Give the extent of all Plasmodium falciparum-infected red blood cells.
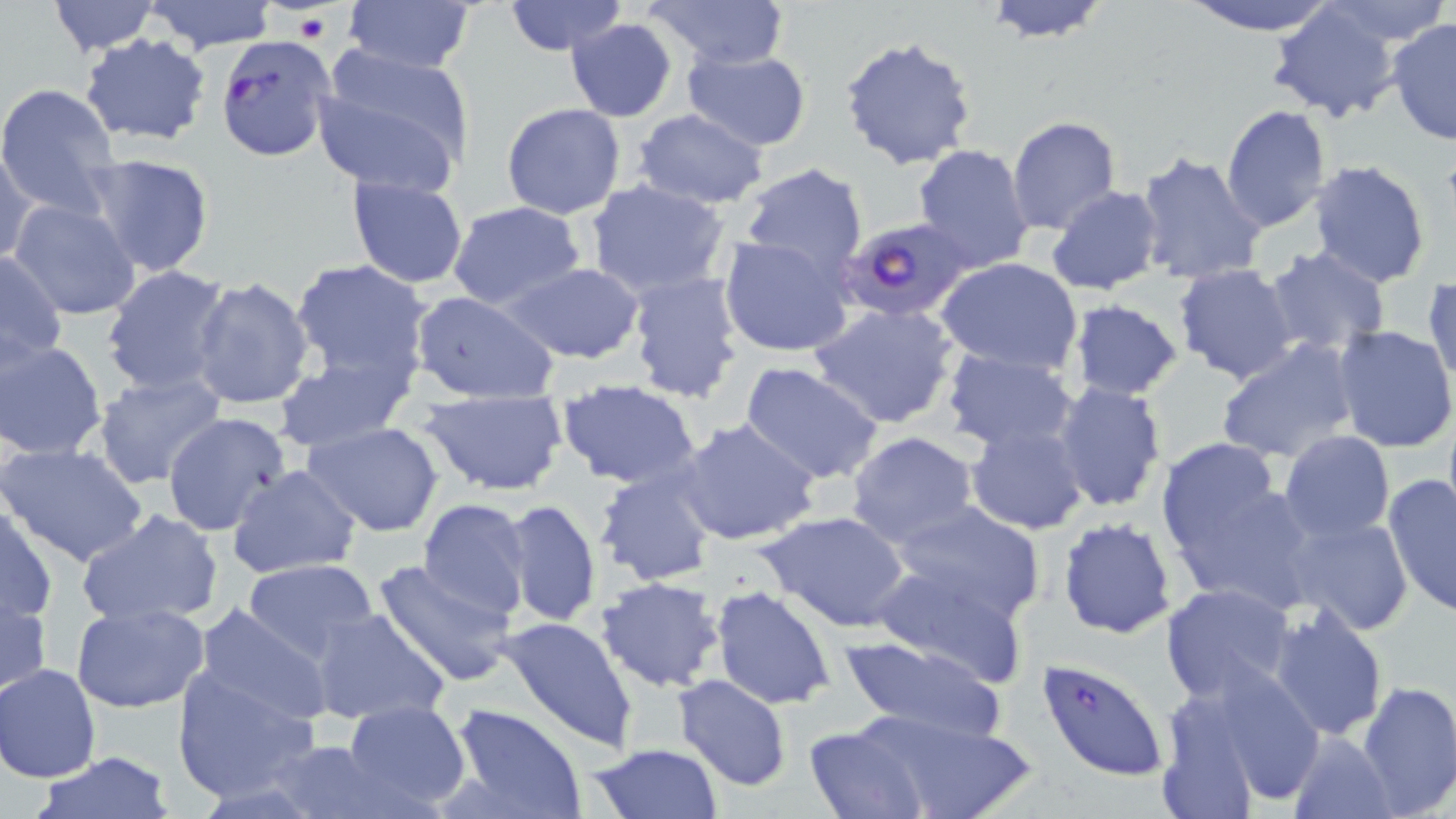
Approximate bounding boxes as (x1,y1)-(x2,y2) corner pairs in pixels.
Plasmodium falciparum-infected red blood cells: (216,35)-(334,161), (838,216)-(974,322), (1037,657)-(1170,782).

slide-level diagnosis = Plasmodium falciparum
uninfected red blood cell locations = approximate bounding boxes as (x1,y1)-(x2,y2) corner pairs in pixels: (47,0)-(162,56), (138,0)-(281,53), (502,0)-(628,55), (644,0)-(789,70), (979,0)-(1115,42), (1179,0)-(1341,36), (342,1)-(477,76), (1319,1)-(1453,48), (1266,4)-(1402,125), (565,16)-(678,121), (1388,17)-(1456,147), (80,34)-(213,147), (839,35)-(977,172), (312,44)-(478,195), (684,48)-(812,152), (0,83)-(121,215), (501,103)-(627,220), (1220,104)-(1332,232), (634,109)-(769,208), (1007,116)-(1121,235), (912,143)-(1037,273), (1,147)-(38,266), (1134,149)-(1269,286), (82,153)-(215,278), (1309,159)-(1431,288), (737,163)-(869,280), (349,174)-(469,288), (584,178)-(732,301), (1045,186)-(1163,296), (9,199)-(142,322), (447,200)-(586,311), (717,235)-(854,359), (1263,246)-(1392,355), (0,253)-(69,368), (935,257)-(1083,377), (289,259)-(433,392), (503,263)-(646,364), (101,264)-(233,396), (1174,264)-(1302,387), (625,271)-(746,404), (1426,273)-(1456,391), (189,277)-(316,413), (412,290)-(557,405), (1063,300)-(1187,401), (808,302)-(959,430), (1332,325)-(1456,451), (1214,338)-(1363,465), (0,339)-(106,461), (938,347)-(1080,454), (274,356)-(412,453), (737,362)-(886,486), (93,371)-(227,489), (556,379)-(704,491), (1052,379)-(1167,513), (417,387)-(569,496), (1442,405)-(1455,529), (162,411)-(291,537), (677,417)-(821,546), (303,420)-(444,537), (965,422)-(1089,534), (845,430)-(984,552), (1278,430)-(1396,543), (1155,440)-(1312,609), (1,442)-(148,567), (227,463)-(363,579), (593,467)-(718,588), (1381,473)-(1455,618), (417,498)-(532,618), (502,498)-(602,628), (888,499)-(1046,622), (1,505)-(57,627), (77,508)-(225,628), (758,510)-(912,633), (1056,516)-(1179,639), (1282,516)-(1414,636), (243,558)-(380,665), (371,559)-(518,688), (873,559)-(1030,688), (595,577)-(726,693), (1160,582)-(1296,703), (0,585)-(51,703), (711,585)-(836,711), (70,603)-(210,714), (192,603)-(336,728), (1267,605)-(1390,741), (307,606)-(450,725), (499,614)-(640,754), (840,633)-(1008,744), (1157,661)-(1324,814), (1,664)-(102,783), (172,665)-(320,806), (675,673)-(792,792), (1355,678)-(1455,818), (341,700)-(472,812), (447,702)-(587,819), (831,704)-(1036,819), (800,724)-(928,818), (1285,730)-(1397,819), (260,739)-(404,819), (585,742)-(724,819), (29,749)-(177,818)
preparation = thin blood film
field of view = single
platelet locations = approximate bounding boxes as (x1,y1)-(x2,y2) corner pairs in pixels: (294,12)-(330,45)
image size = 1456×819 pixels
modality = light microscopy
stain = May-Grünwald-Giemsa
magnification = 1000x